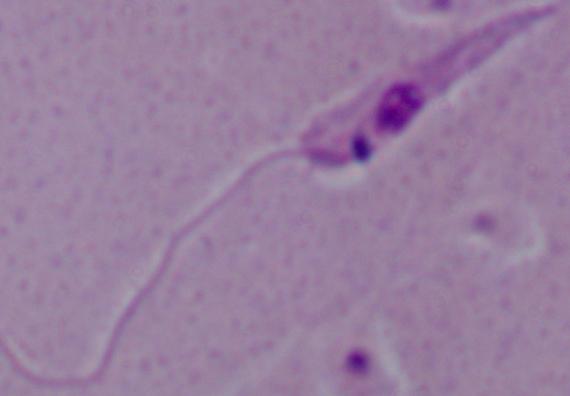
identification: Leishmania
modality: micrograph
magnification: 1000x